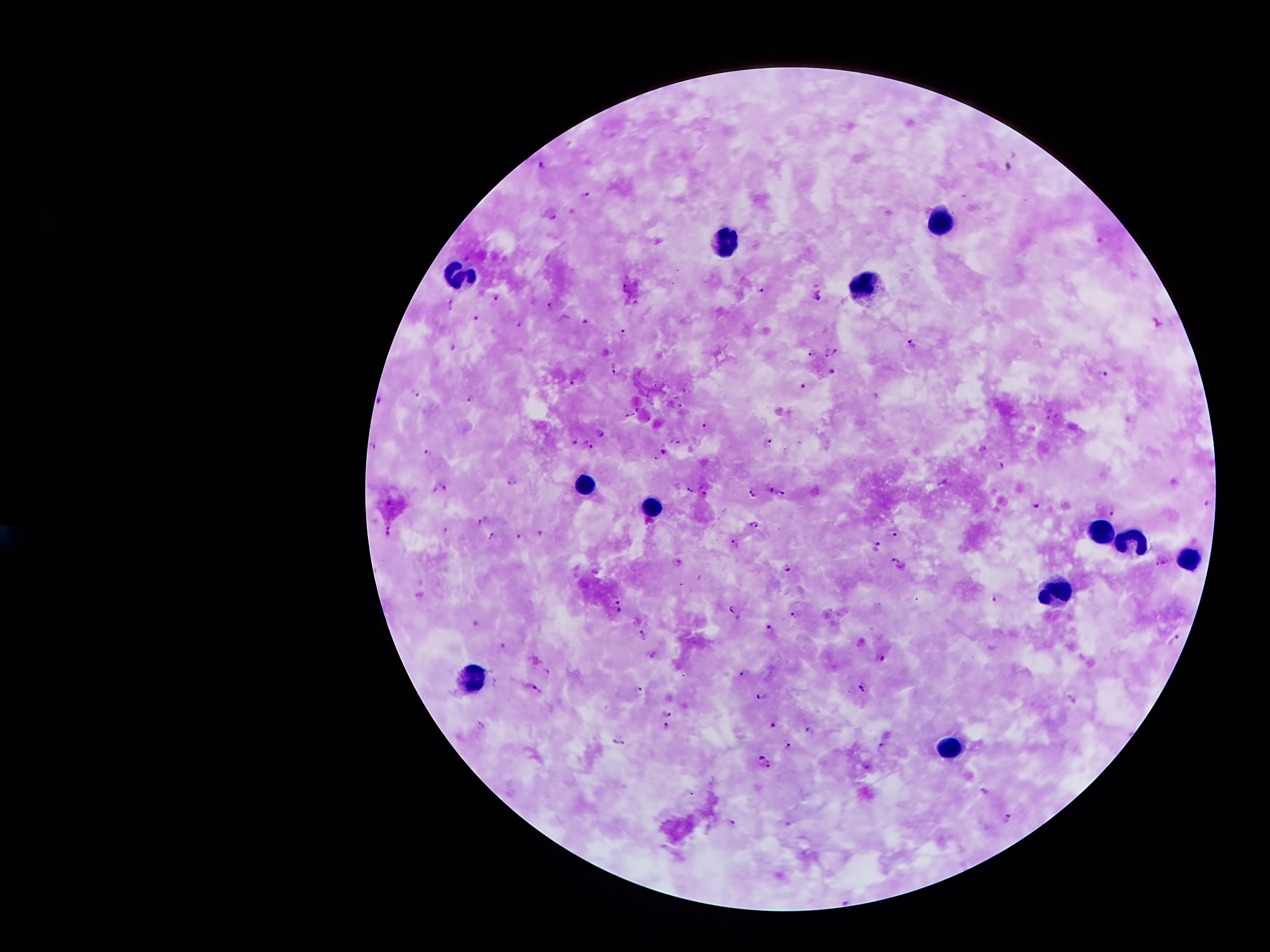

Approximate centers as (x, y) in pixels. Leukocyte locations: (941, 220), (727, 247), (462, 283), (863, 284), (587, 485), (653, 509), (1099, 529), (1134, 539), (1190, 562), (1056, 589), (477, 675), (954, 747). Plasmodium parasite locations: (542, 164), (586, 195), (555, 218), (625, 286), (760, 292), (818, 293), (496, 297), (636, 303), (452, 304), (549, 305), (477, 319), (584, 321), (521, 323), (624, 331), (913, 343), (830, 351), (812, 352), (616, 369), (832, 371), (1104, 376), (573, 383), (804, 386), (417, 393), (471, 399), (380, 401), (630, 414), (704, 425), (601, 432), (575, 440), (767, 442), (589, 443), (370, 446), (428, 452), (663, 452), (1001, 465), (513, 481), (702, 486), (443, 488), (771, 489), (690, 491), (783, 493), (704, 494), (753, 494), (1208, 505), (1037, 506), (1111, 511), (482, 522), (754, 524), (389, 530), (894, 533), (539, 534), (491, 535), (519, 535), (735, 544), (878, 547), (894, 559), (1159, 562), (787, 566), (996, 597), (617, 600), (733, 608), (619, 610), (795, 614), (773, 627), (644, 635), (1176, 640), (503, 645), (880, 658), (745, 672), (864, 686), (538, 690), (640, 690), (760, 696), (668, 712), (774, 724), (666, 727), (810, 730), (620, 743), (883, 744), (787, 746), (767, 761), (869, 768), (985, 790), (1007, 817), (735, 822). Smartphone photograph taken through the microscope eyepiece. Image is 1270×952 pixels. Giemsa-stained preparation. Thick peripheral-blood smear. 100x magnification. One field from this slide. Patient malaria status: infected with Plasmodium falciparum.